Outline each Plasmodium vivax-infected red blood cell.
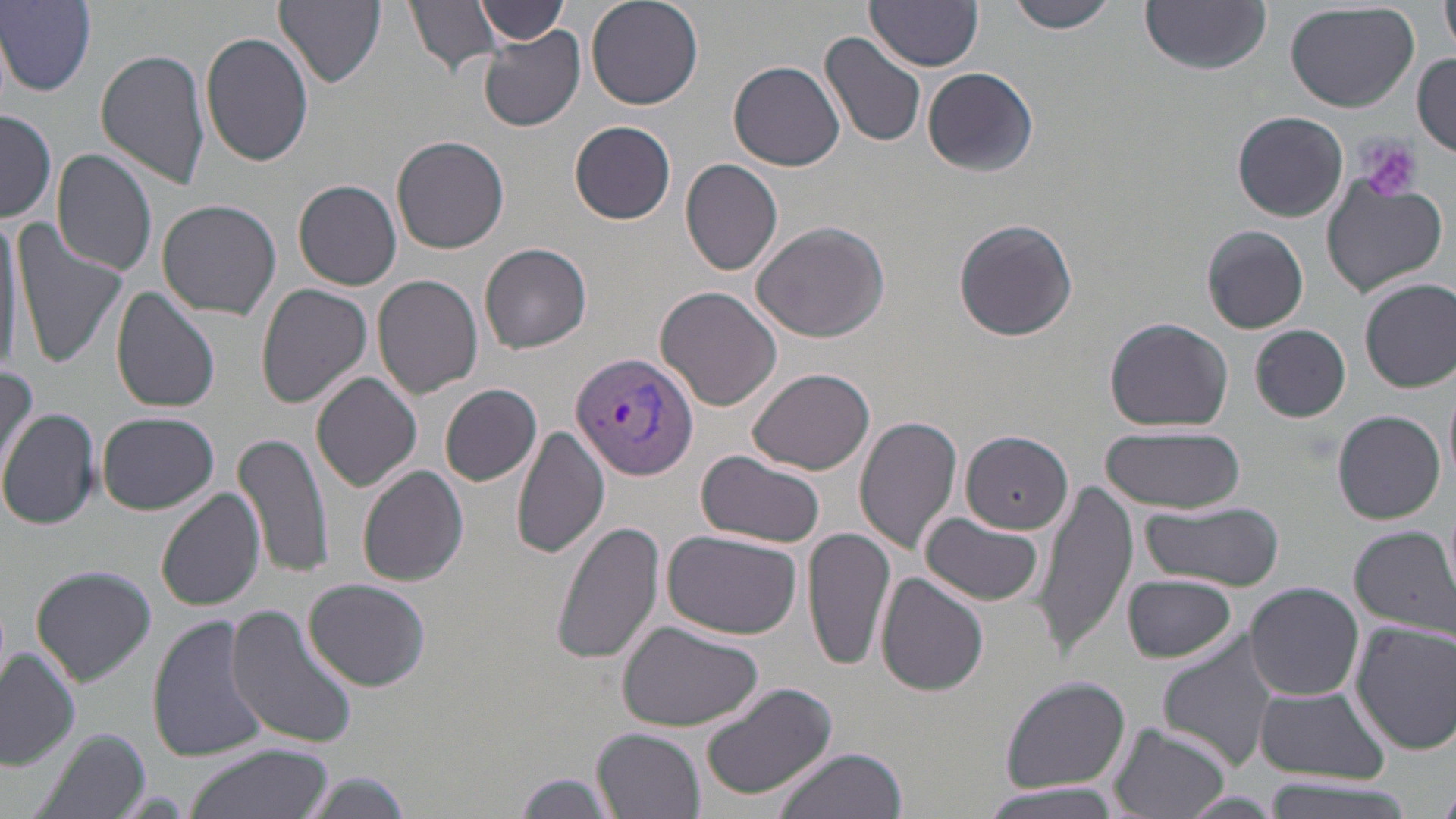

Approximate bounding boxes as (x1,y1)-(x2,y2) corner pairs in pixels.
Plasmodium vivax-infected red blood cells: (571,350)-(698,481).

Platelet locations: (1357,136)-(1423,204). Uninfected red blood cell locations: (274,0)-(386,90), (405,0)-(506,75), (474,0)-(564,46), (586,0)-(704,110), (867,0)-(986,70), (1008,0)-(1121,34), (1142,0)-(1272,73), (1440,0)-(1456,56), (1,1)-(97,95), (1285,1)-(1419,113), (478,29)-(586,133), (200,30)-(316,167), (819,32)-(929,150), (94,48)-(211,189), (1412,54)-(1456,157), (729,61)-(845,170), (922,64)-(1040,176), (1,108)-(56,223), (1233,111)-(1348,221), (569,121)-(677,224), (391,136)-(509,254), (52,148)-(158,279), (680,159)-(785,276), (294,179)-(403,290), (1322,179)-(1448,296), (157,199)-(280,319), (0,208)-(28,373), (953,217)-(1078,340), (11,219)-(128,371), (752,221)-(889,341), (1203,225)-(1308,334), (480,240)-(592,352), (373,274)-(483,399), (1360,278)-(1456,392), (256,283)-(373,407), (656,285)-(783,411), (110,287)-(221,413), (1103,315)-(1235,431), (1249,325)-(1351,423), (0,364)-(38,476), (748,368)-(874,473), (312,372)-(423,493), (441,384)-(542,485), (0,408)-(99,529), (1333,410)-(1446,524), (96,411)-(221,515), (853,413)-(962,557), (512,424)-(609,559), (1101,426)-(1247,514), (234,428)-(336,582), (960,430)-(1074,533), (696,449)-(827,549), (357,466)-(468,587), (1035,480)-(1137,654), (157,486)-(264,610), (1140,499)-(1285,591), (920,514)-(1045,606), (551,520)-(668,666), (1347,524)-(1456,635), (802,526)-(896,672), (662,529)-(803,638), (812,554)-(964,692), (31,567)-(156,685), (876,573)-(990,696), (1122,573)-(1237,662), (302,579)-(431,692), (1246,581)-(1363,700), (226,606)-(358,749), (147,613)-(268,763), (616,621)-(765,733), (1350,621)-(1456,756), (1156,634)-(1283,770), (0,648)-(79,771), (998,677)-(1131,795), (699,680)-(841,801), (1252,682)-(1391,781), (1109,723)-(1233,819), (592,727)-(705,819), (31,730)-(150,819), (182,744)-(333,819), (769,748)-(908,819), (295,771)-(413,818), (512,773)-(618,816), (1261,776)-(1419,817), (975,780)-(1125,818), (1177,792)-(1283,818). Slide-level diagnosis: Plasmodium vivax. Image is 1456×819 pixels. Thin blood smear. Optical microscopy. May-Grünwald-Giemsa stain. One field of a larger specimen. 1000x magnification.